Classify this cell by malaria status.
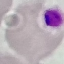
Uninfected.

image type = cell patch, automatically extracted from a larger field of view and resized to 64 × 64 pixels
capture = smartphone camera at the microscope eyepiece
preparation = thin smear
stain = Giemsa